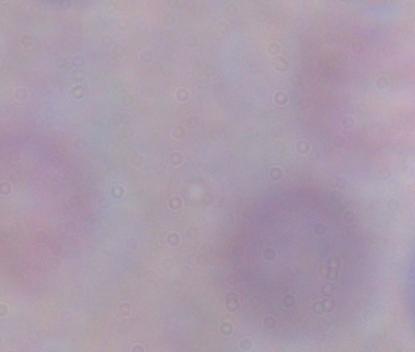 Captured at 1000x magnification. Photomicrograph. A trypanosome is shown.